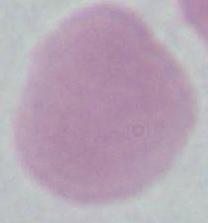 Micrograph. An erythrocyte is shown. Captured at 1000x magnification.